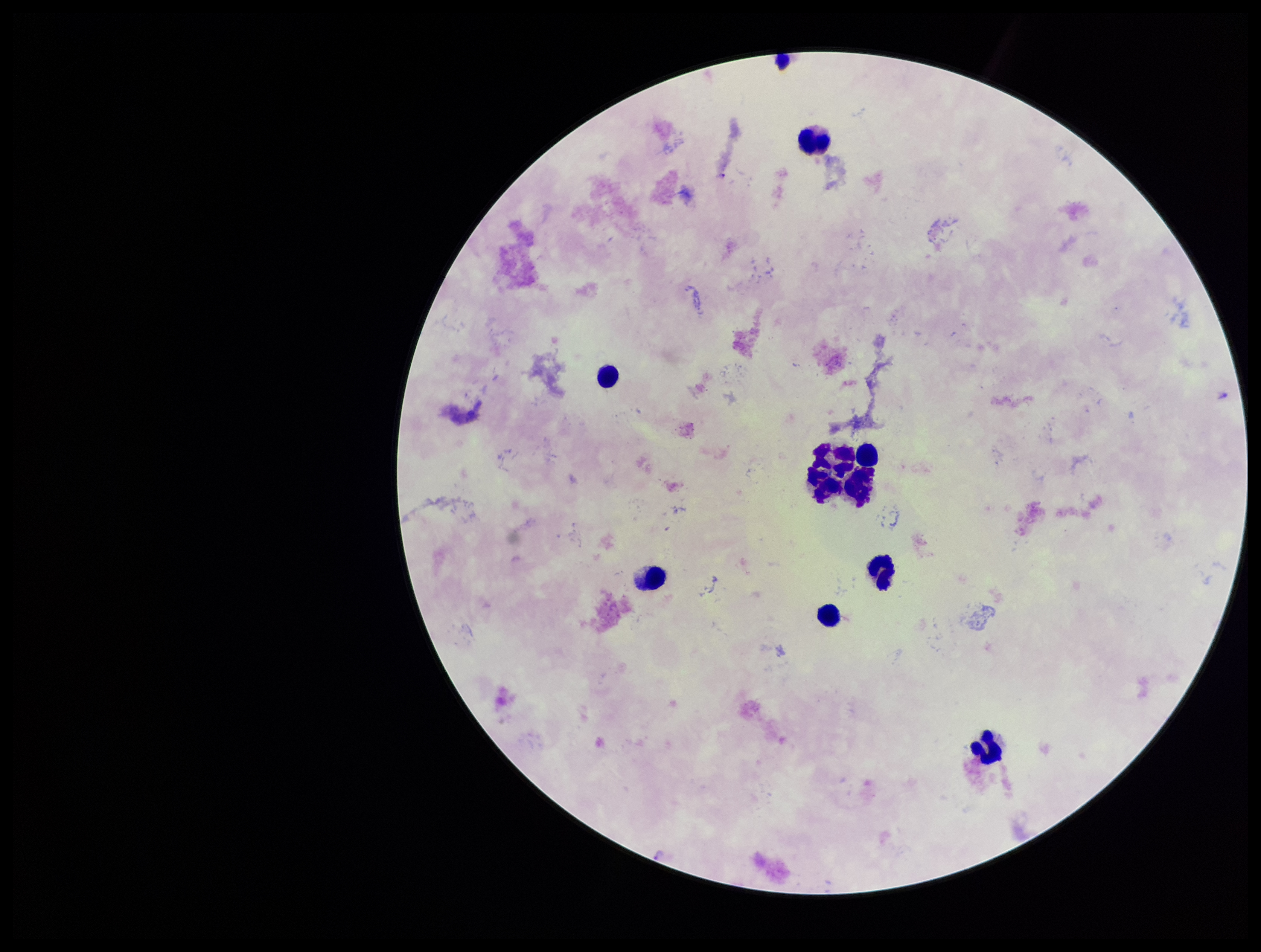

leukocyte count = 10
image size = 1261×952 pixels
stain = Giemsa
parasite count = 1
Plasmodium parasites = identified
capture = smartphone photograph through the microscope eyepiece
species reported for this patient = Plasmodium falciparum
patient malaria status = infected
field of view = single
preparation = thick smear